Give the position of every malaria parasite, noting whether each is a trophozoite, schizont, or gametocyte.
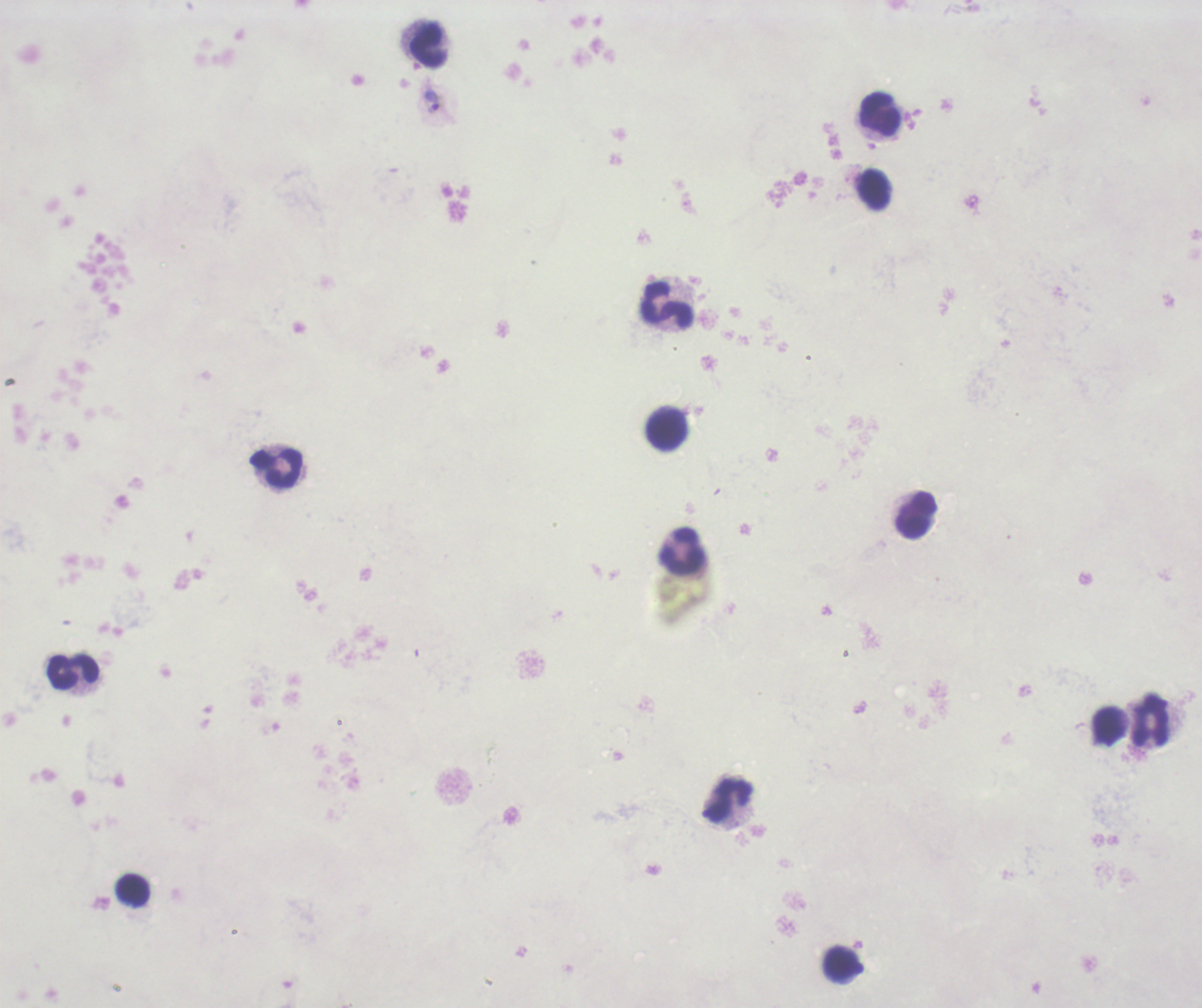
Approximate object centers, in pixels from the top-left corner.
Trophozoites: (x=436, y=100).
No schizont or gametocyte forms observed.

{
  "coloration_quality": "bad",
  "stain": "Romanowsky",
  "image_size": "1202×1008 pixels",
  "preparation": "thick smear of blood",
  "context": "previously used in a real diagnosis",
  "magnification": "100x",
  "field_of_view": "single",
  "leukocyte_locations": "approximate object centers, in pixels from the top-left corner: (x=428, y=45), (x=881, y=114), (x=872, y=188), (x=667, y=304), (x=665, y=428), (x=276, y=469), (x=916, y=515), (x=681, y=551), (x=74, y=672), (x=1150, y=719), (x=1107, y=726), (x=729, y=801), (x=132, y=890), (x=840, y=964)",
  "background_quality": "unsatisfactory"
}